State which cell type is depicted.
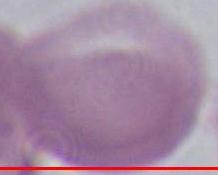

This is an erythrocyte.

magnification = 1000x
modality = micrograph